Report the malaria status of this cell.
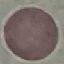

It is uninfected.

Summary:
  - Capture: smartphone through the microscope eyepiece
  - Preparation: thin smear
  - Stain: Giemsa
  - Image type: automatically extracted cell patch, resized to 64 × 64 pixels